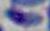 Toxoplasma gondii is shown. 1000x magnification. Photomicrograph.